Identify the parasite.
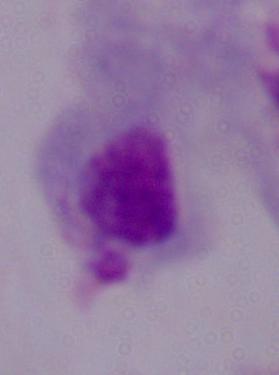
This is a trichomonad.

magnification: 1000x
modality: photomicrograph